Assess for Plasmodium parasites.
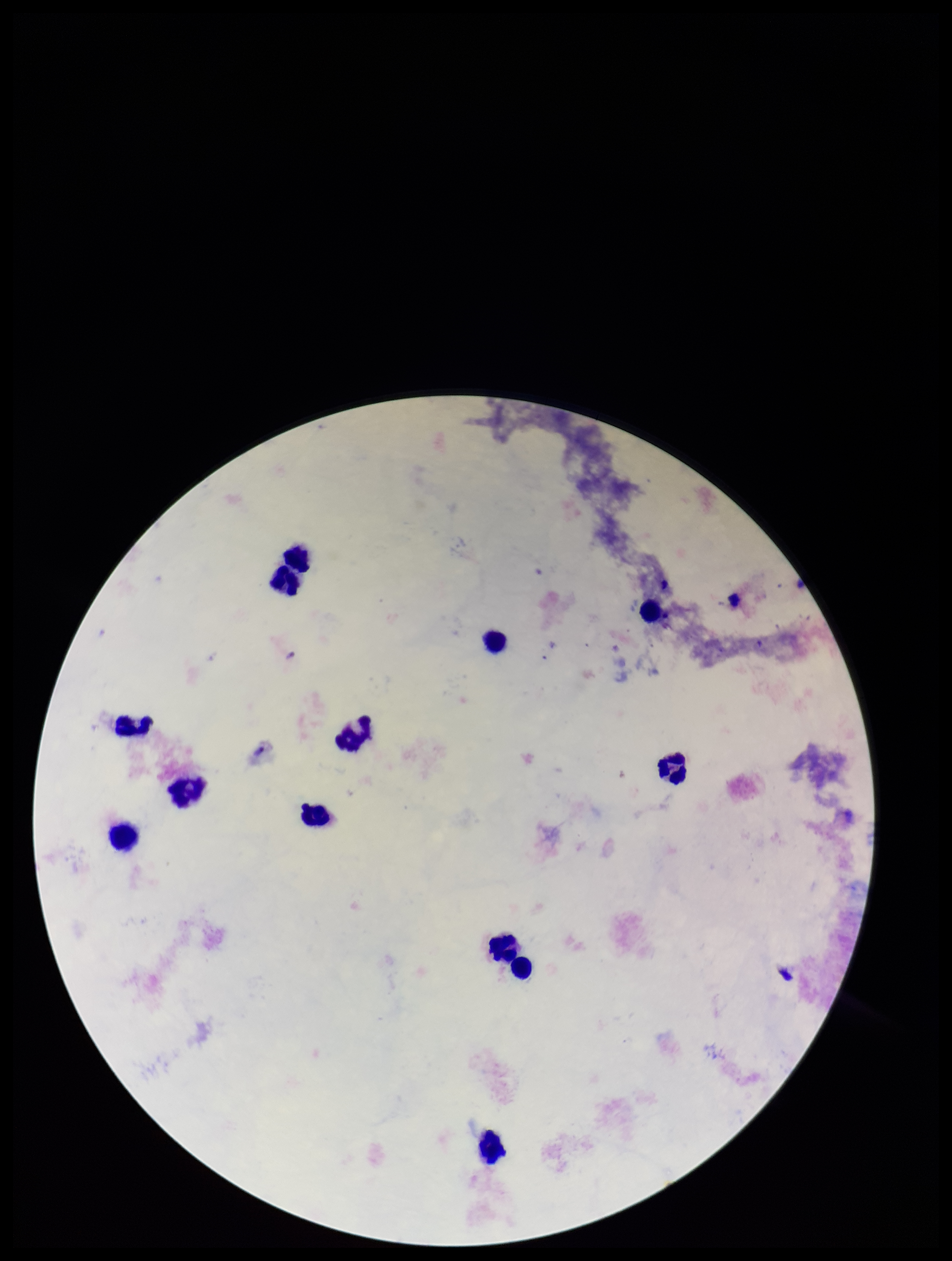
None identified.

Parasite count: 0. Stained with Giemsa. Patient malaria status: negative. Single field of view. Image is 952×1261 pixels. Preparation: thick. Leukocyte count: 13. Smartphone photograph taken through the eyepiece of a microscope.